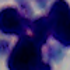

{
  "modality": "micrograph",
  "magnification": "1000x",
  "identification": "leukocyte"
}